Give the position of every malaria parasite.
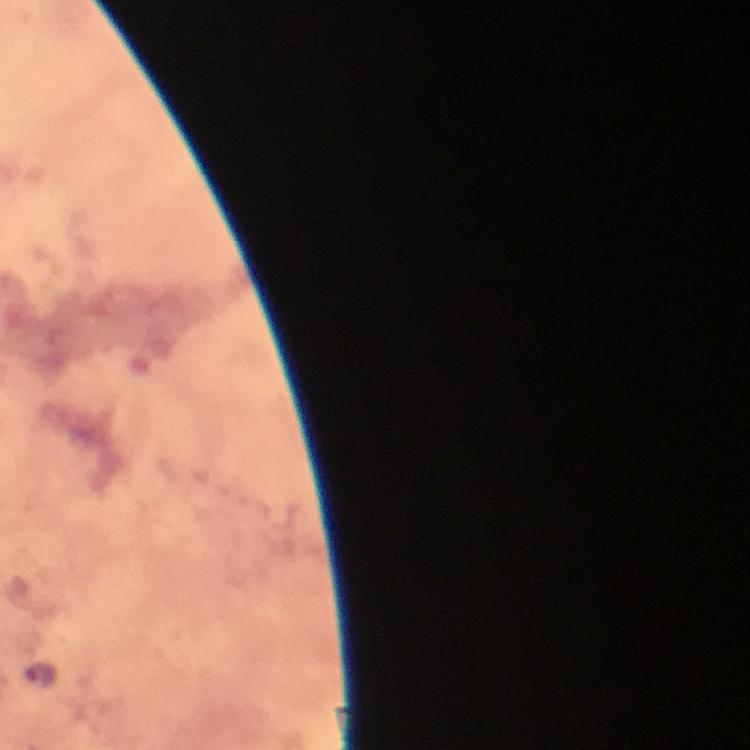
Approximate centers as [x, y] in pixels.
Malaria parasites: [40, 674].

stain = Giemsa
cropped from = one field of view
capture = smartphone camera through the microscope
preparation = thick smear
context = from a diagnostic examination for malaria
immersion oil = applied
image size = 750×750 pixels
magnification = 100x